Locate every Plasmodium falciparum parasite and give its life-cycle stage, and locate every leukocyte and any debris.
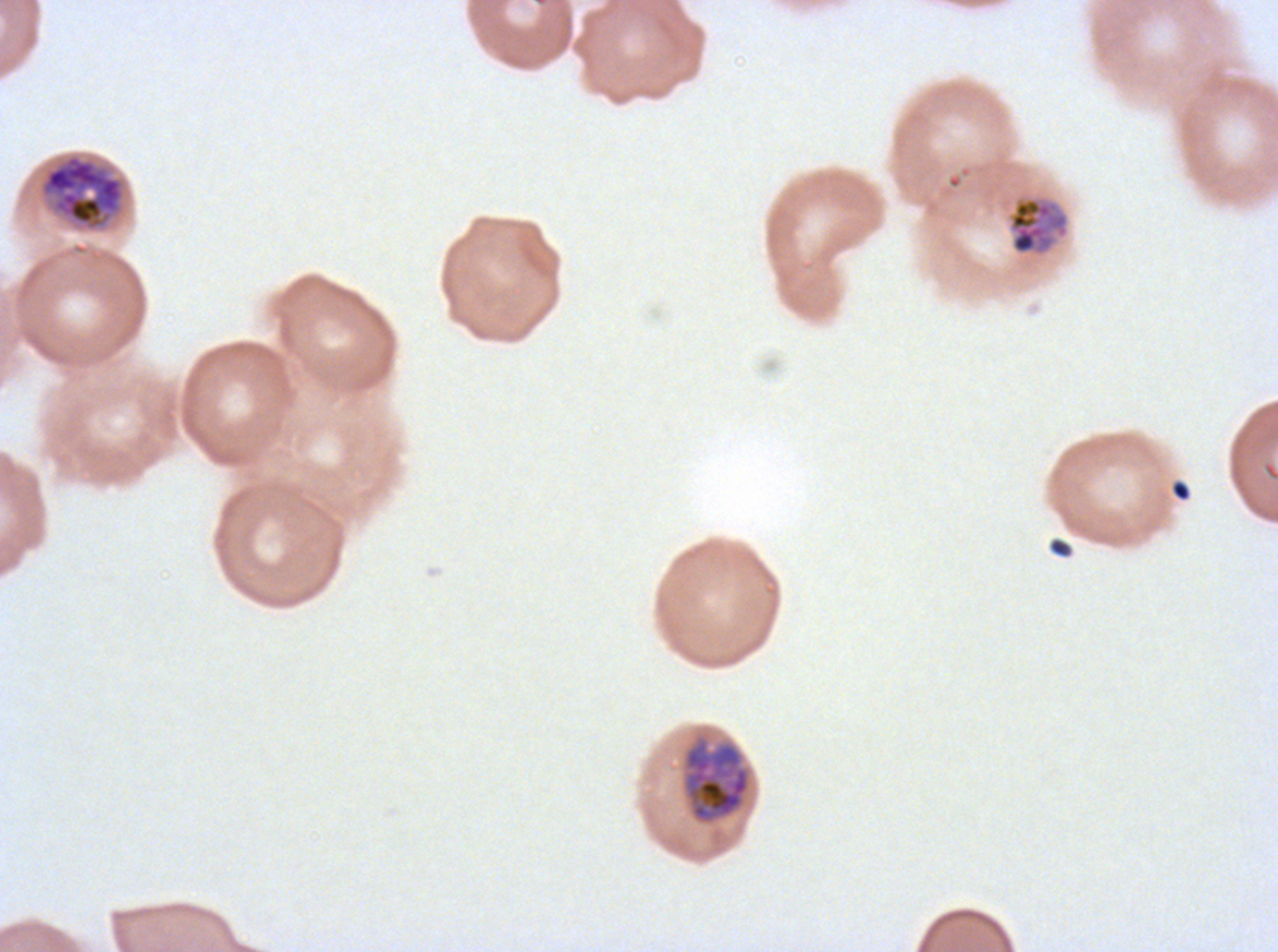
Approximate bounding boxes as [x1, y1, x2, y2] in pixels.
Mid trophozoites: [1007, 195, 1070, 257].
Late trophozoites: [40, 153, 125, 230], [684, 740, 750, 823].
Debris: [1171, 480, 1191, 502], [1048, 537, 1073, 558].
No rings, late-ring/early-trophozoite forms, early schizonts, late schizonts, segmenters, gametocytes, or leukocytes observed.

Giemsa stain. Life-cycle stages observed: mid trophozoite, late trophozoite. Thin blood smear. Image is 1278×952 pixels. Plasmodium falciparum from a patient in The Gambia, cultured ex vivo for 24 to 48 hours. A sub-image separated from a larger composite.